Assess for malaria.
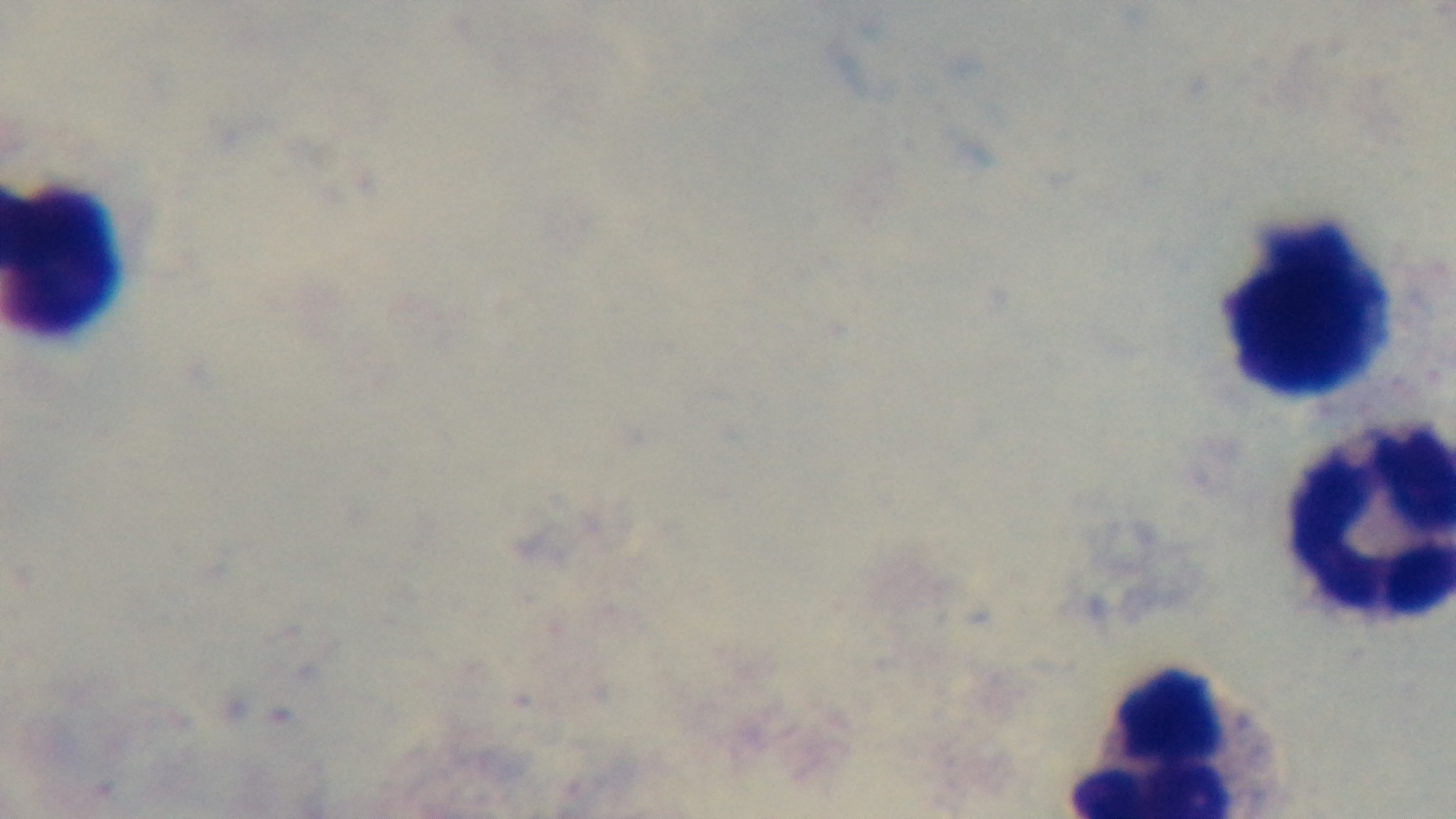
It is uninfected.

Mounted 4K digital camera. Giemsa stain. One field from the slide. Preparation: thick blood film. Oil-immersion objective, 100x. Light microscopy.